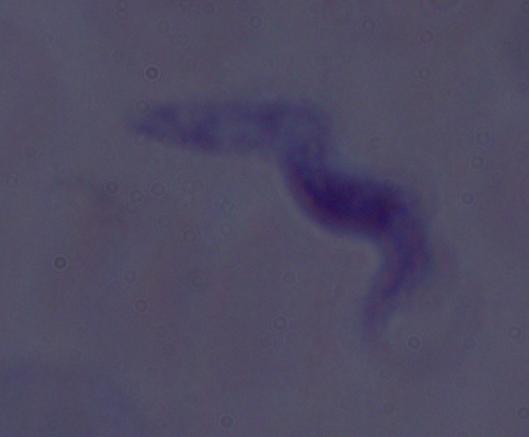

Summary:
  - Magnification: 1000x
  - Identification: trypanosome
  - Modality: photomicrograph